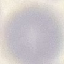
Summary:
  - Result: no malaria parasites seen
  - Capture: smartphone through the microscope eyepiece
  - Image type: cell patch, automatically extracted from a larger field of view and resized to 64 × 64 pixels
  - Stain: Giemsa
  - Preparation: thin smear